Locate every leukocyte (white blood cell).
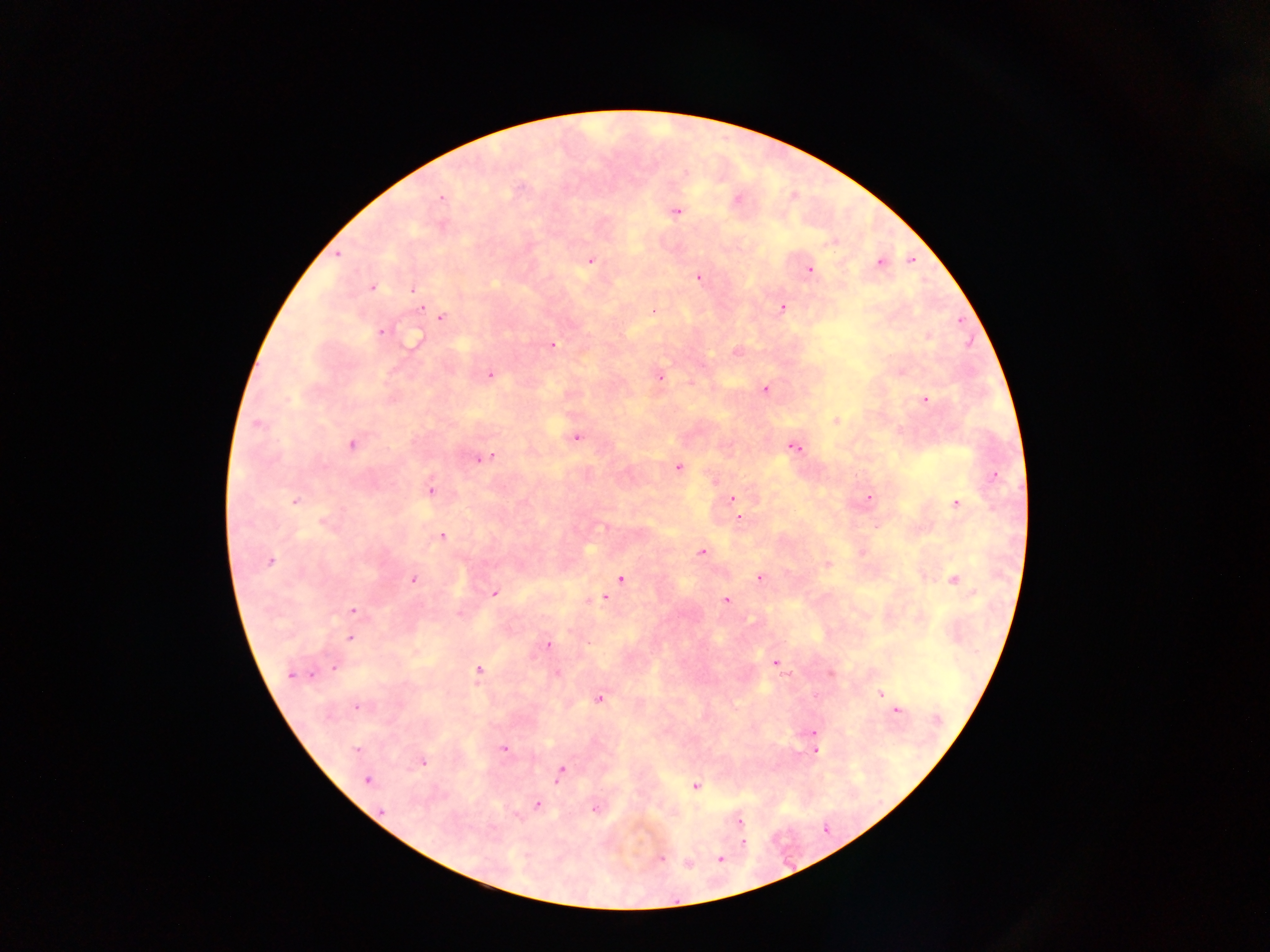

No leukocytes observed.

Approximate centers as (x, y) in pixels.
Summary:
  - Plasmodium parasite locations: (442, 198), (737, 199), (677, 212), (338, 254), (911, 260), (590, 261), (880, 262), (810, 270), (699, 278), (372, 287), (414, 290), (782, 308), (653, 310), (442, 318), (381, 331), (927, 337), (414, 341), (553, 344), (490, 373), (660, 377), (764, 389), (925, 400), (836, 421), (257, 424), (576, 436), (351, 444), (794, 447), (483, 459), (678, 467), (994, 476), (431, 489), (868, 498), (732, 499), (295, 500), (956, 503), (740, 518), (323, 523), (605, 527), (442, 537), (702, 552), (270, 563), (827, 564), (760, 578), (413, 579), (621, 579), (954, 580), (495, 594), (603, 598), (725, 600), (352, 610), (460, 613), (350, 639), (548, 644), (775, 663), (335, 668), (479, 670), (557, 673), (831, 673), (291, 674), (881, 694), (600, 699), (886, 699), (358, 706), (897, 711), (813, 733), (504, 748), (356, 749), (815, 749), (422, 762), (561, 772), (367, 779), (696, 785), (537, 804), (595, 809), (381, 810), (740, 822), (742, 842), (661, 858), (720, 858), (687, 864)
  - Image size: 1270×952 pixels
  - Capture: mobile-phone photograph through a microscope
  - Country: Ghana
  - Preparation: thick blood film
  - Field of view: single